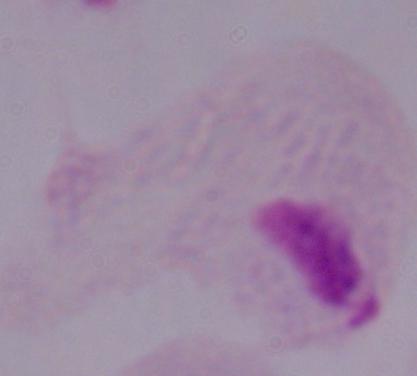

Summary:
  - Modality: photomicrograph
  - Identification: trichomonad
  - Magnification: 1000x